Classify this cell by malaria status.
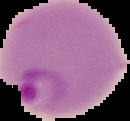
It is parasitized.

Cell region segmented out of the field of view; the surrounding area is masked to black. Image is 130×121 pixels. From a thin blood film.